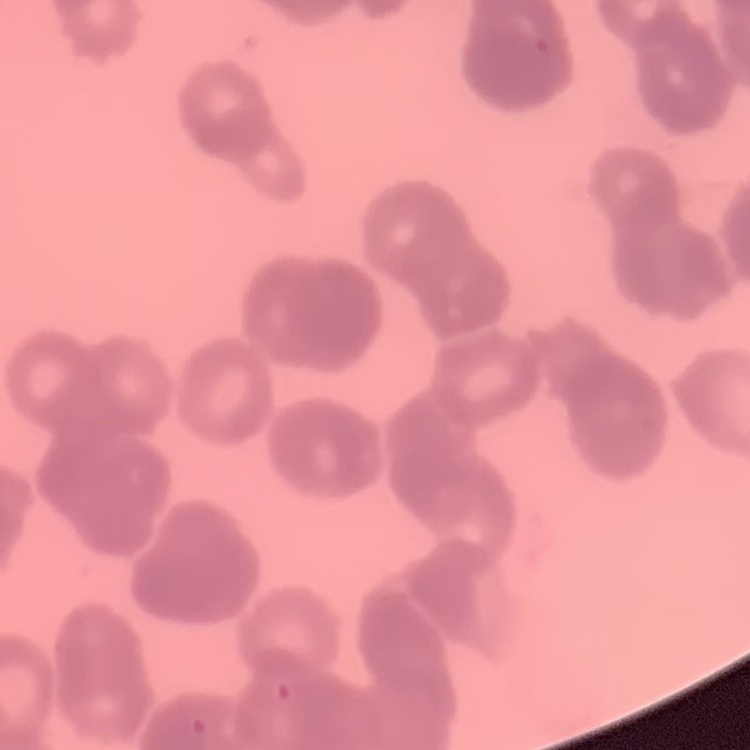
erythrocyte morphology = rouleaux formation
image type = square crop of a larger photomicrograph
preparation = thin blood film
stain = Field's or Giemsa